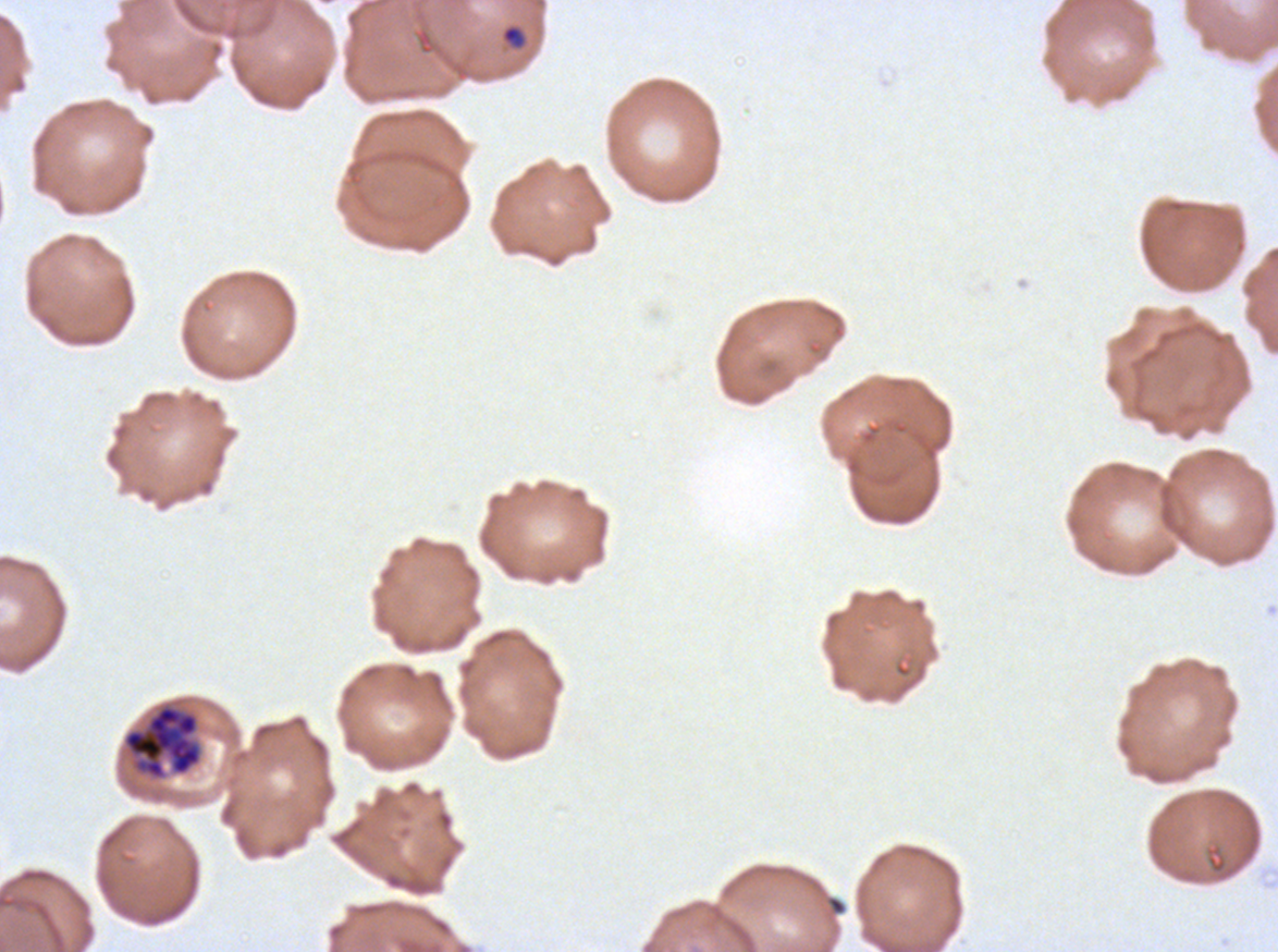

notation = approximate bounding rectangles given as corner coordinates in pixels from the top-left
late schizont locations = (x1=121, y1=702, x2=203, y2=781)
ring locations = (x1=501, y1=25, x2=525, y2=48)
stain = Giemsa
specimen = Plasmodium falciparum from a patient in The Gambia, cultured ex vivo for 24 to 48 hours
preparation = thin blood smear
image size = 1278×952 pixels
field of view = sub-image separated from a larger composite
life-cycle stages observed = ring, late schizont